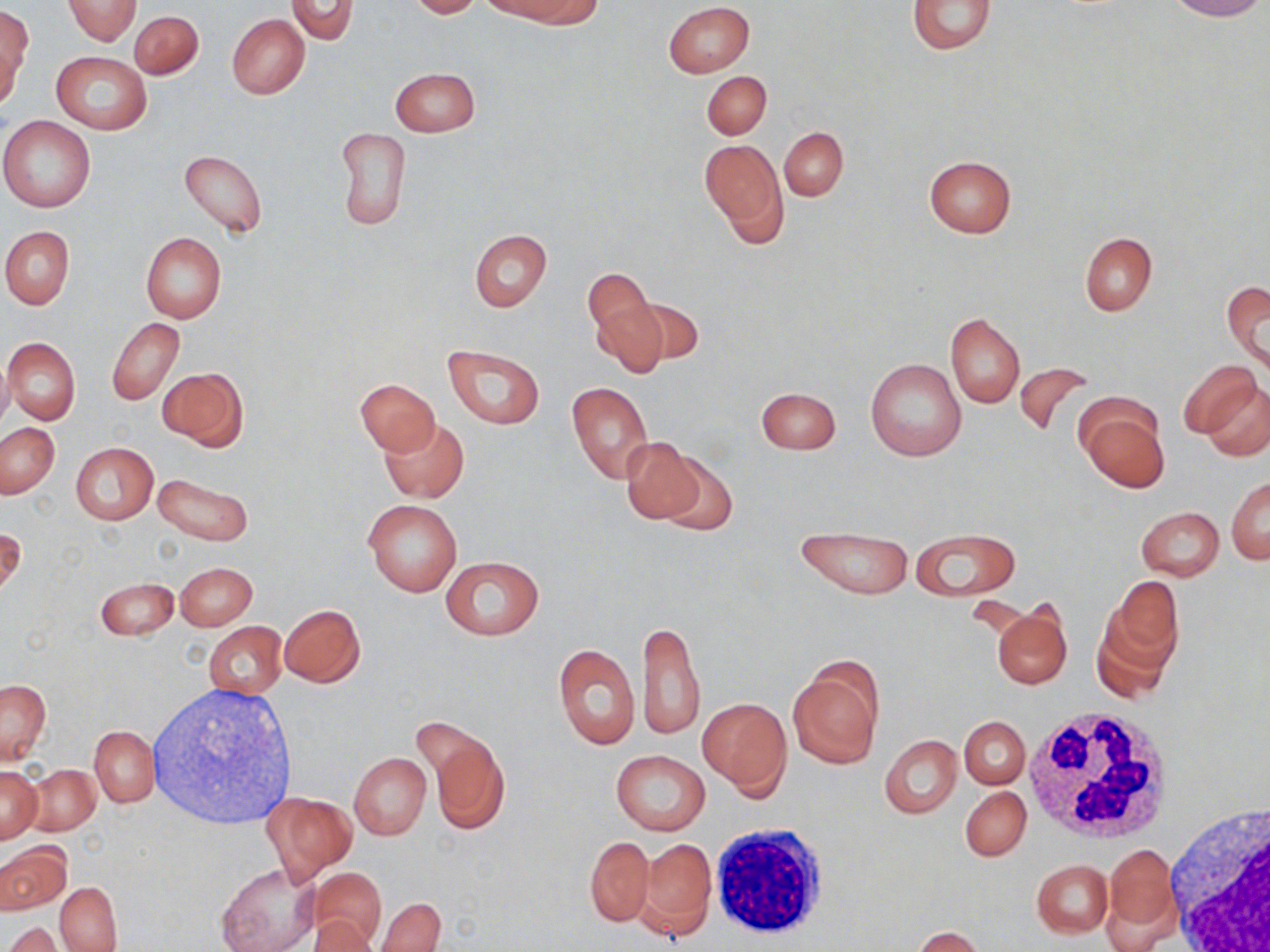

Summary:
  - Coordinate format: approximate bounding boxes as [x1, y1, x2, y2] in pixels
  - White blood cell locations (subset): [1021, 709, 1174, 845], [710, 822, 832, 942]
  - Uninfected red blood cell locations (subset): [63, 0, 141, 44], [286, 0, 358, 43], [409, 0, 485, 18], [907, 0, 995, 54], [1165, 0, 1266, 21], [512, 1, 604, 28], [664, 2, 755, 78], [1, 6, 32, 102], [129, 10, 203, 79], [226, 14, 309, 99], [51, 52, 152, 133], [390, 67, 480, 136], [702, 71, 770, 139], [0, 115, 97, 212], [779, 127, 849, 200], [335, 128, 412, 230], [700, 139, 785, 238], [178, 149, 268, 238], [924, 154, 1017, 239], [1, 226, 74, 309], [469, 229, 551, 312], [1080, 231, 1156, 315], [141, 233, 226, 323], [583, 266, 654, 338], [1222, 278, 1270, 375], [623, 296, 704, 368], [591, 301, 670, 378], [945, 311, 1024, 407], [107, 317, 184, 405], [3, 338, 81, 425], [444, 344, 545, 430], [0, 355, 11, 434], [865, 358, 967, 463], [1179, 358, 1263, 443], [1013, 361, 1094, 437], [157, 367, 247, 450], [356, 378, 439, 454], [1201, 380, 1269, 462], [566, 381, 653, 483], [755, 387, 841, 454], [1076, 398, 1169, 492], [380, 418, 469, 503], [0, 422, 60, 498], [620, 437, 704, 523], [70, 442, 158, 525], [656, 453, 739, 536], [152, 472, 253, 546], [1227, 476, 1269, 564], [364, 499, 461, 597], [1136, 505, 1224, 581], [795, 525, 913, 600], [0, 526, 25, 597], [911, 528, 1018, 601], [439, 554, 546, 641], [175, 562, 257, 630], [1105, 576, 1185, 671], [95, 577, 179, 641], [279, 604, 365, 687], [993, 605, 1072, 689], [1092, 607, 1179, 699], [637, 618, 705, 740], [204, 622, 287, 698], [553, 643, 639, 749], [789, 661, 883, 767], [0, 677, 51, 764], [699, 697, 791, 795], [960, 716, 1030, 788], [90, 725, 158, 806], [426, 730, 510, 835], [880, 735, 961, 818], [611, 749, 709, 834], [349, 752, 431, 839], [26, 764, 101, 834], [0, 765, 42, 842], [960, 786, 1030, 861], [261, 791, 356, 881], [586, 835, 653, 926], [639, 838, 717, 939], [1102, 842, 1179, 947], [1, 843, 71, 914], [1032, 859, 1113, 937], [217, 862, 320, 952], [310, 869, 385, 946], [55, 882, 122, 951], [375, 897, 445, 952], [309, 916, 376, 952], [4, 922, 64, 952], [911, 927, 985, 952]
  - Slide-level diagnosis: no evidence of blood parasites
  - Image size: 1270×952 pixels
  - Preparation: thin blood smear
  - Modality: optical microscopy
  - Stain: May-Grünwald-Giemsa
  - Field of view: single
  - Magnification: 1000x